Point out every Plasmodium parasite.
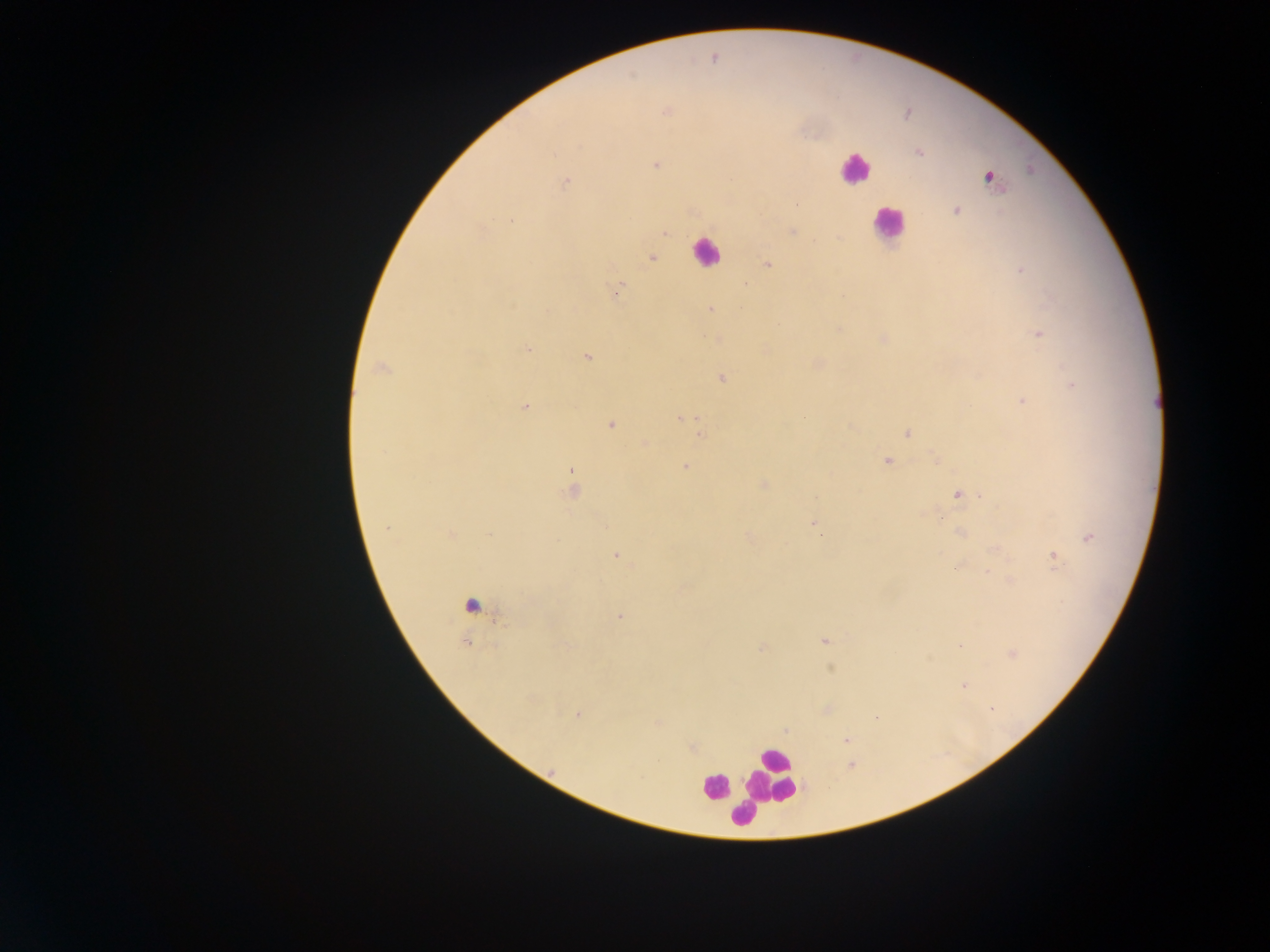

Approximate centers as (x, y) in pixels.
Plasmodium parasites: (919, 153), (656, 164), (1029, 169), (988, 177), (566, 181), (957, 209), (662, 232), (652, 258), (766, 264), (1020, 269), (615, 290), (512, 306), (709, 307), (1038, 334), (528, 350), (586, 357), (379, 368), (722, 376), (1071, 384), (1022, 400), (525, 406), (678, 418), (802, 418), (612, 423), (908, 433), (702, 435), (886, 462), (687, 465), (571, 472), (763, 485), (571, 493), (956, 495), (982, 496), (814, 522), (606, 526), (387, 529), (959, 532), (451, 533), (488, 534), (1086, 537), (750, 538), (614, 555), (1053, 556), (958, 566), (986, 572), (1010, 578), (621, 615), (823, 641), (960, 646), (564, 647), (759, 647), (1011, 654), (930, 658), (829, 669), (962, 686), (579, 714), (576, 717), (658, 723), (846, 739), (692, 748), (553, 774).

image size = 1270×952 pixels
country = Ghana
field of view = single
leukocyte locations = approximate centers as (x, y) in pixels: (853, 168), (889, 224), (707, 254), (776, 759), (773, 776), (716, 787), (743, 816)
capture = mobile-phone photograph through a microscope
preparation = thick blood film